Give the extent of all Plasmodium vivax-infected red blood cells.
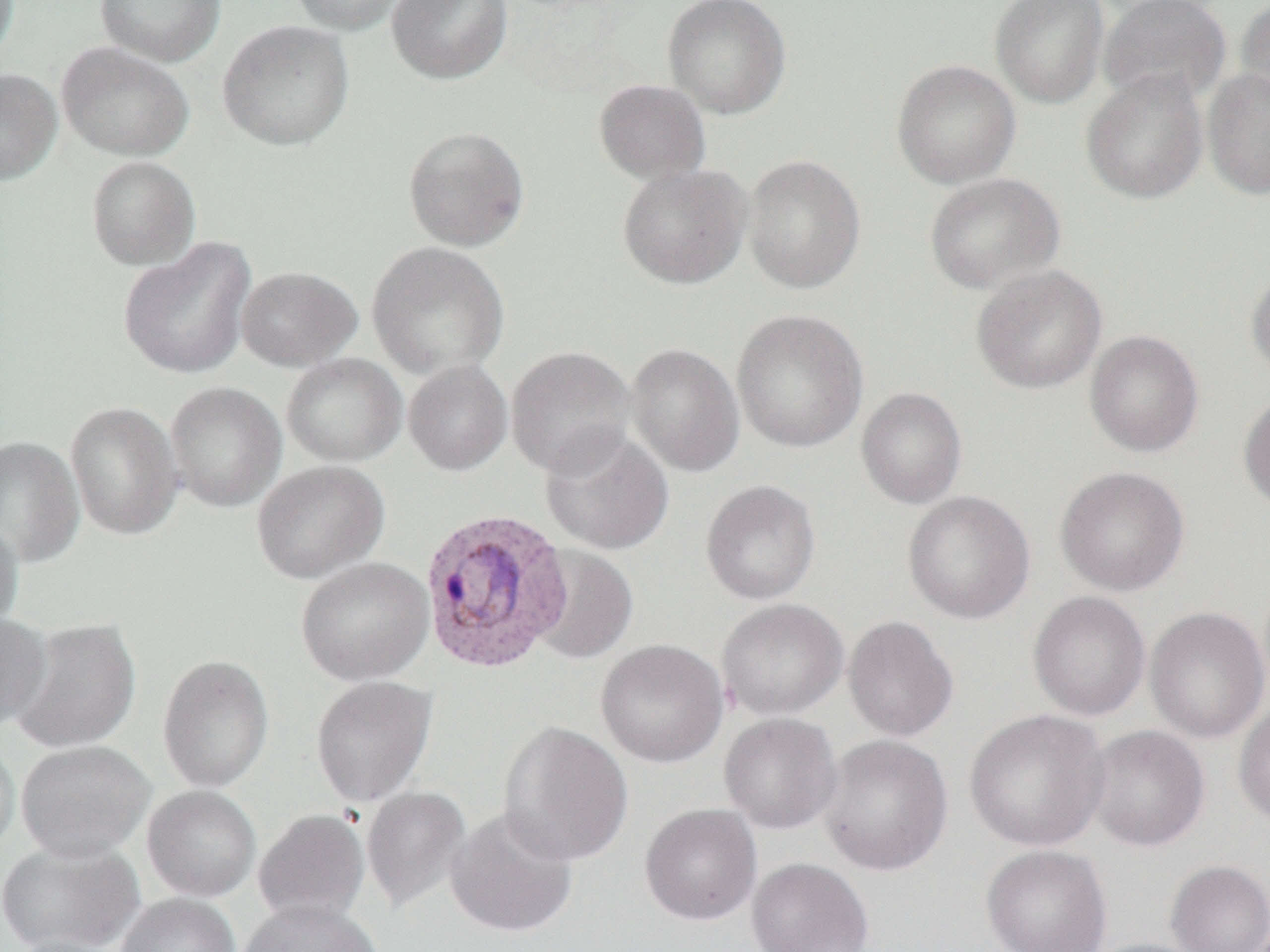
Approximate bounding boxes as [x1, y1, x2, y2] in pixels.
Plasmodium vivax-infected red blood cells: [418, 509, 574, 674].

Summary:
  - Uninfected red blood cell locations: [95, 0, 225, 66], [290, 0, 410, 35], [386, 0, 511, 84], [663, 0, 792, 118], [990, 0, 1110, 108], [1099, 0, 1231, 107], [1236, 0, 1270, 114], [217, 19, 354, 150], [56, 42, 194, 161], [891, 59, 1021, 189], [1202, 67, 1270, 200], [0, 69, 62, 185], [1081, 70, 1209, 204], [593, 79, 711, 185], [403, 125, 530, 251], [743, 154, 866, 294], [85, 156, 201, 270], [617, 163, 751, 289], [924, 172, 1065, 295], [118, 237, 256, 380], [367, 241, 509, 379], [971, 265, 1106, 394], [236, 266, 363, 371], [1246, 266, 1270, 383], [731, 309, 869, 454], [1084, 330, 1204, 458], [625, 343, 745, 477], [506, 345, 636, 477], [281, 353, 407, 467], [403, 360, 512, 476], [165, 381, 287, 512], [856, 387, 967, 509], [1238, 393, 1270, 514], [65, 401, 184, 540], [541, 428, 674, 555], [0, 435, 84, 568], [251, 460, 389, 584], [1055, 467, 1190, 596], [700, 480, 821, 605], [902, 490, 1035, 624], [0, 519, 24, 636], [529, 546, 638, 664], [295, 557, 434, 685], [1027, 591, 1151, 721], [716, 598, 848, 720], [1144, 606, 1269, 743], [0, 611, 53, 732], [842, 615, 959, 742], [9, 617, 141, 754], [596, 639, 728, 768], [157, 654, 275, 793], [310, 675, 437, 807], [1233, 700, 1270, 828], [964, 709, 1110, 852], [718, 713, 843, 834], [497, 721, 634, 866], [1086, 724, 1209, 852], [0, 734, 20, 859], [817, 734, 953, 876], [16, 740, 155, 861], [142, 785, 261, 902], [361, 786, 471, 912], [640, 803, 762, 925], [445, 807, 579, 938], [253, 809, 370, 926], [0, 840, 144, 952], [981, 845, 1112, 952], [746, 857, 874, 952], [1165, 860, 1270, 952], [116, 892, 240, 952], [237, 899, 384, 952], [6, 935, 126, 952], [1079, 938, 1214, 952]
  - Slide-level diagnosis: Plasmodium vivax
  - Image size: 1270×952 pixels
  - Preparation: thin blood smear
  - Magnification: 1000x
  - Field of view: single
  - Modality: optical microscopy